Classify this cell by malaria status.
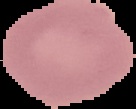
Uninfected.

image size = 136×109 pixels
image type = segmented cell region on a black background
preparation = thin blood smear